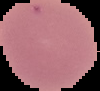 Segmented cell region on a black background. From a thin blood film. Image is 100×91 pixels. Result: no malaria parasites detected.